Comment on the morphology of the red blood cells.
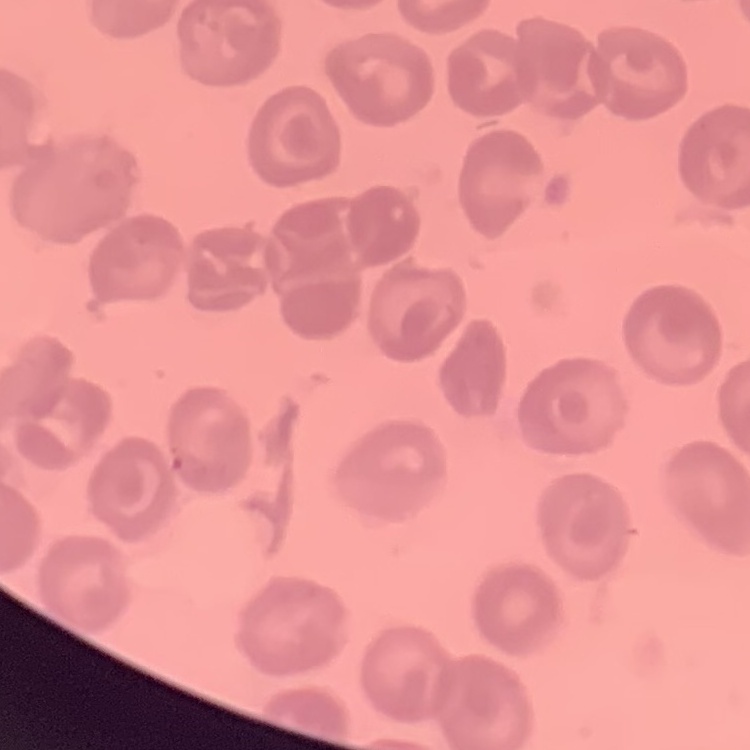

No rouleaux formation.

stain = Field's or Giemsa
preparation = thin blood film
image type = square crop of a larger photomicrograph